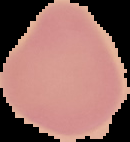

image type = segmented cell region with the area outside set to black
image size = 130×142 pixels
malaria status = uninfected
preparation = thin blood film